Give the extent of all Plasmodium falciparum-infected red blood cells.
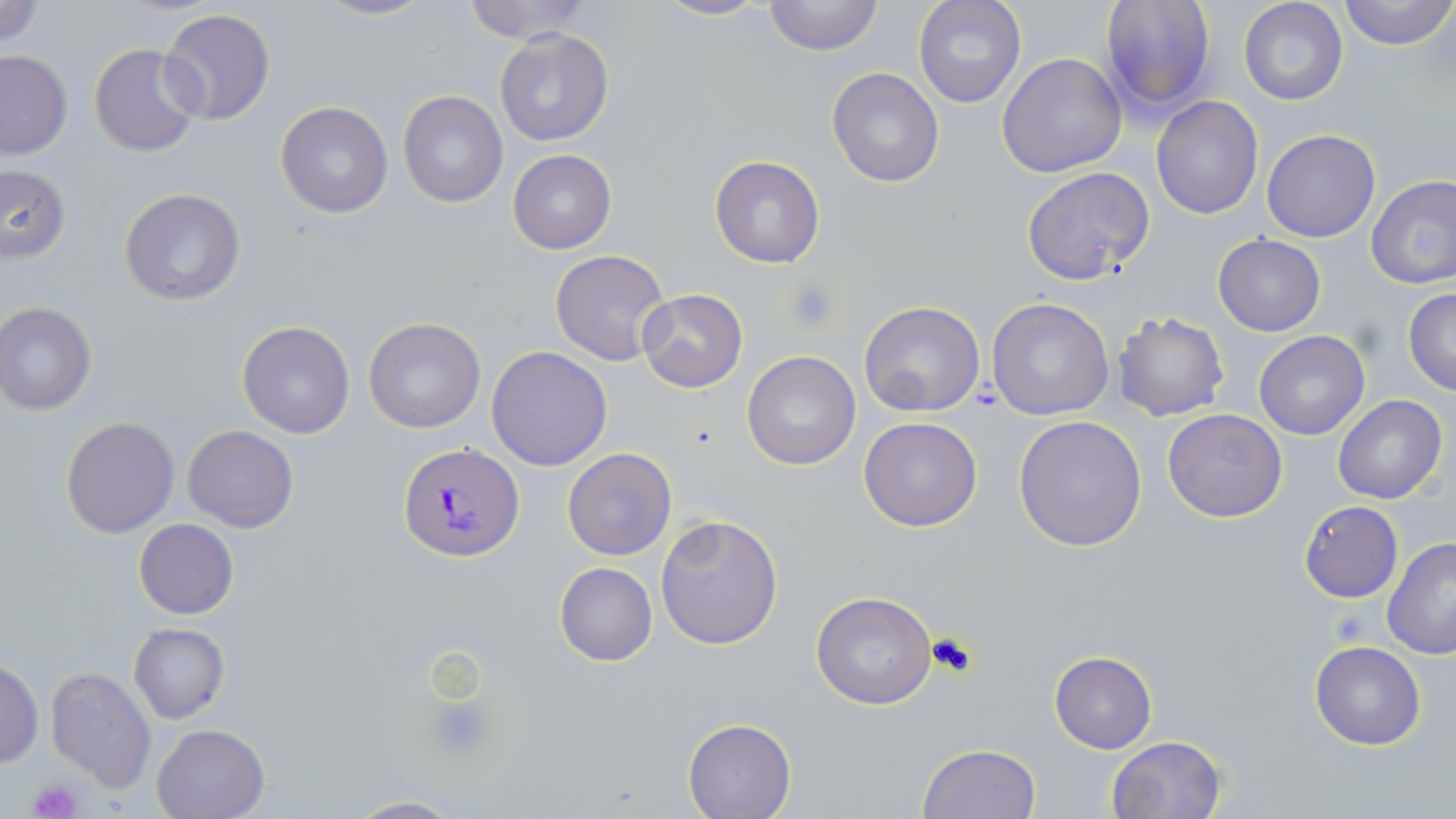
Approximate bounding boxes as [x1, y1, x2, y2] in pixels.
Plasmodium falciparum-infected red blood cells: [399, 443, 524, 563].

{
  "slide_level_diagnosis": "Plasmodium falciparum",
  "uninfected_red_blood_cell_locations": "approximate bounding boxes as [x1, y1, x2, y2] in pixels: [0, 0, 47, 49], [313, 0, 436, 22], [458, 0, 595, 43], [653, 0, 774, 21], [764, 0, 882, 56], [913, 0, 1027, 108], [1099, 0, 1218, 113], [1338, 0, 1456, 51], [1238, 1, 1349, 106], [158, 8, 276, 126], [494, 27, 615, 147], [89, 42, 203, 158], [0, 48, 72, 159], [997, 52, 1128, 176], [826, 67, 944, 187], [397, 91, 508, 207], [1151, 97, 1263, 220], [276, 102, 394, 219], [1261, 129, 1381, 243], [508, 150, 616, 254], [710, 156, 824, 268], [0, 165, 71, 263], [1020, 166, 1154, 285], [1366, 175, 1456, 291], [119, 188, 245, 307], [1213, 235, 1326, 336], [551, 249, 672, 366], [637, 288, 747, 393], [1402, 288, 1456, 395], [986, 298, 1115, 420], [859, 301, 985, 417], [0, 302, 97, 415], [1112, 311, 1229, 422], [364, 317, 486, 434], [237, 319, 356, 439], [1254, 331, 1370, 440], [486, 345, 613, 471], [742, 350, 861, 469], [1334, 396, 1446, 505], [1162, 408, 1287, 522], [1013, 415, 1147, 551], [61, 417, 178, 537], [859, 417, 982, 531], [182, 424, 300, 532], [563, 449, 676, 561], [1299, 500, 1403, 602], [655, 514, 784, 650], [134, 518, 238, 618], [1382, 537, 1456, 659], [554, 562, 657, 665], [811, 591, 938, 710], [128, 623, 229, 724], [1309, 641, 1427, 750], [1050, 651, 1157, 753], [0, 660, 44, 767], [45, 665, 157, 792], [683, 718, 795, 818], [151, 722, 271, 818], [1106, 735, 1227, 819], [917, 744, 1041, 818], [343, 795, 464, 818]",
  "magnification": "1000x",
  "stain": "May-Grünwald-Giemsa",
  "preparation": "thin blood film",
  "platelet_locations": "approximate bounding boxes as [x1, y1, x2, y2] in pixels: [784, 276, 846, 334], [427, 697, 494, 761], [28, 780, 81, 818]",
  "modality": "optical microscopy",
  "field_of_view": "one of a larger specimen",
  "image_size": "1456×819 pixels"
}